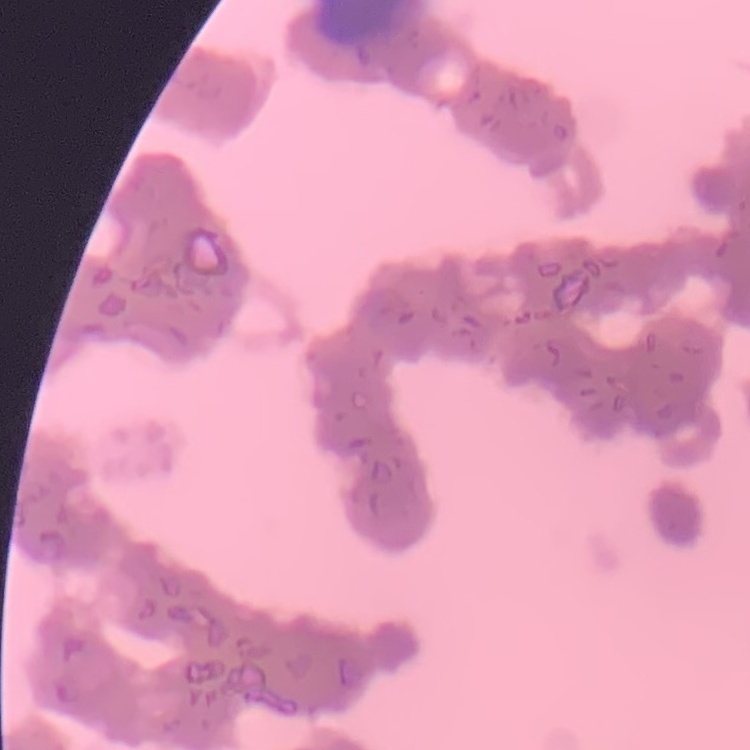

Summary:
  - Red blood cell morphology: rouleaux formation
  - Preparation: thin blood film
  - Image type: square crop of a larger photomicrograph
  - Stain: Field's or Giemsa